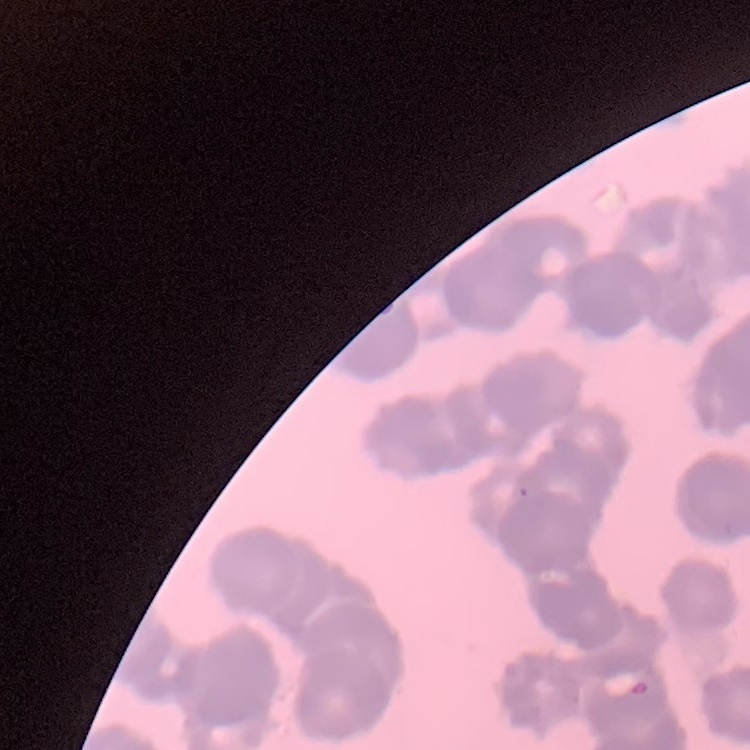
red blood cell morphology = rouleaux formation
stain = Field's or Giemsa
preparation = thin peripheral smear
image type = one tile cut from a larger photomicrograph